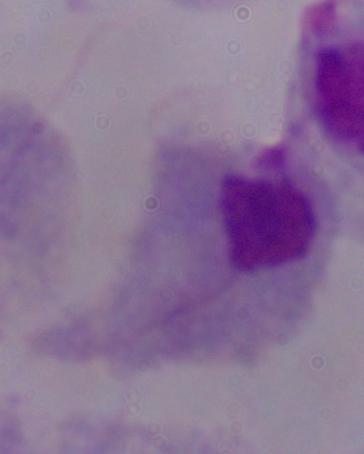

Summary:
  - Magnification: 1000x
  - Modality: photomicrograph
  - Identification: trichomonad